Name the cell type shown.
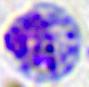
A leukocyte.

400x magnification. Photomicrograph.